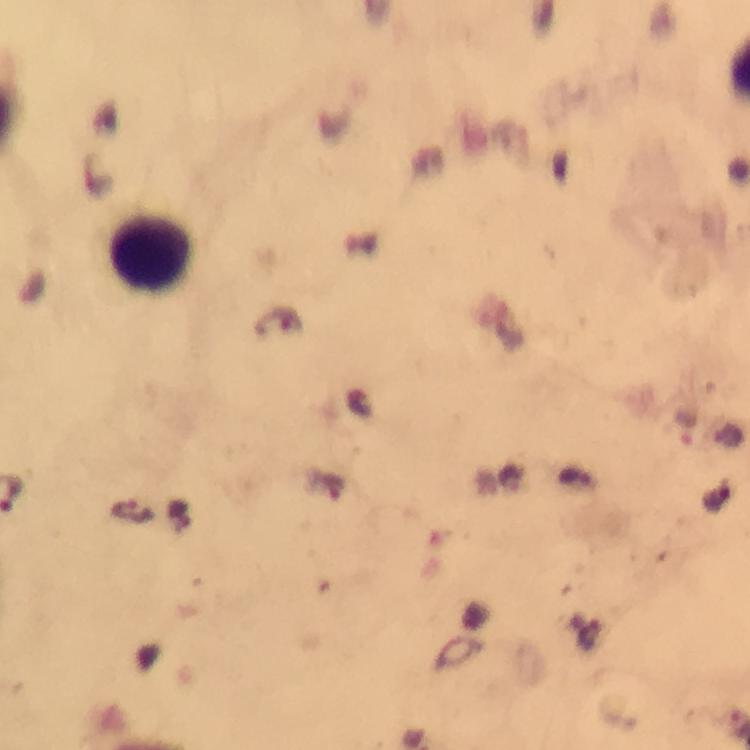
immersion oil = used
Plasmodium parasites = none detected
leukocyte locations = approximate centers as [x, y] in pixels: [151, 256]
stain = Giemsa
cropped from = one field of view
preparation = thick blood smear
image size = 750×750 pixels
magnification = 100x
context = from a diagnostic examination for malaria
capture = smartphone mounted on the microscope